Comment on the morphology of the red blood cells.
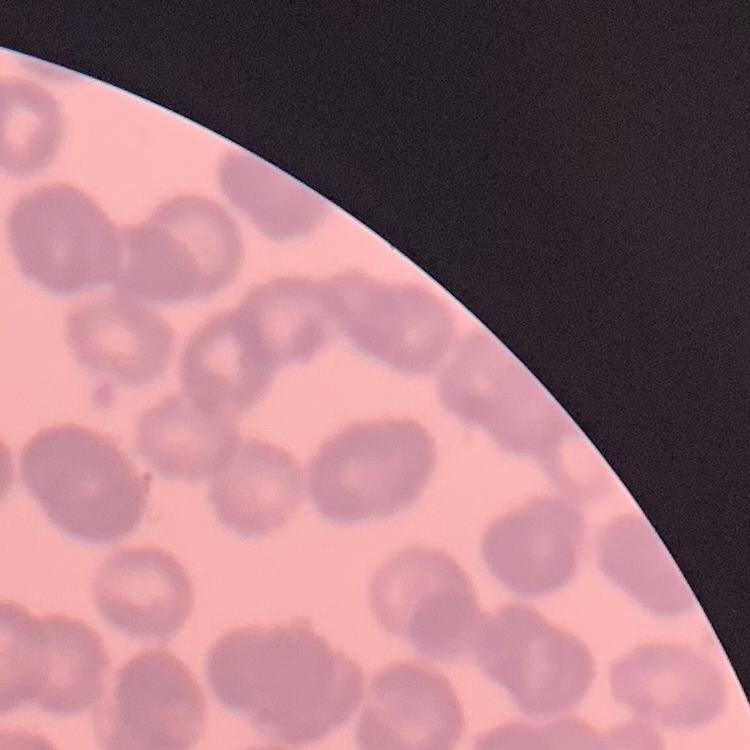
They show rouleaux formation.

Square crop of a larger photomicrograph. Field's or Giemsa stain. Thin blood smear.